Assess this cell for malaria.
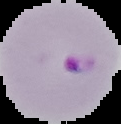

It is parasitized.

preparation = thin blood smear
image size = 121×124 pixels
image type = cell region segmented out of the field of view; surrounding area masked to black